Give the preparation type.
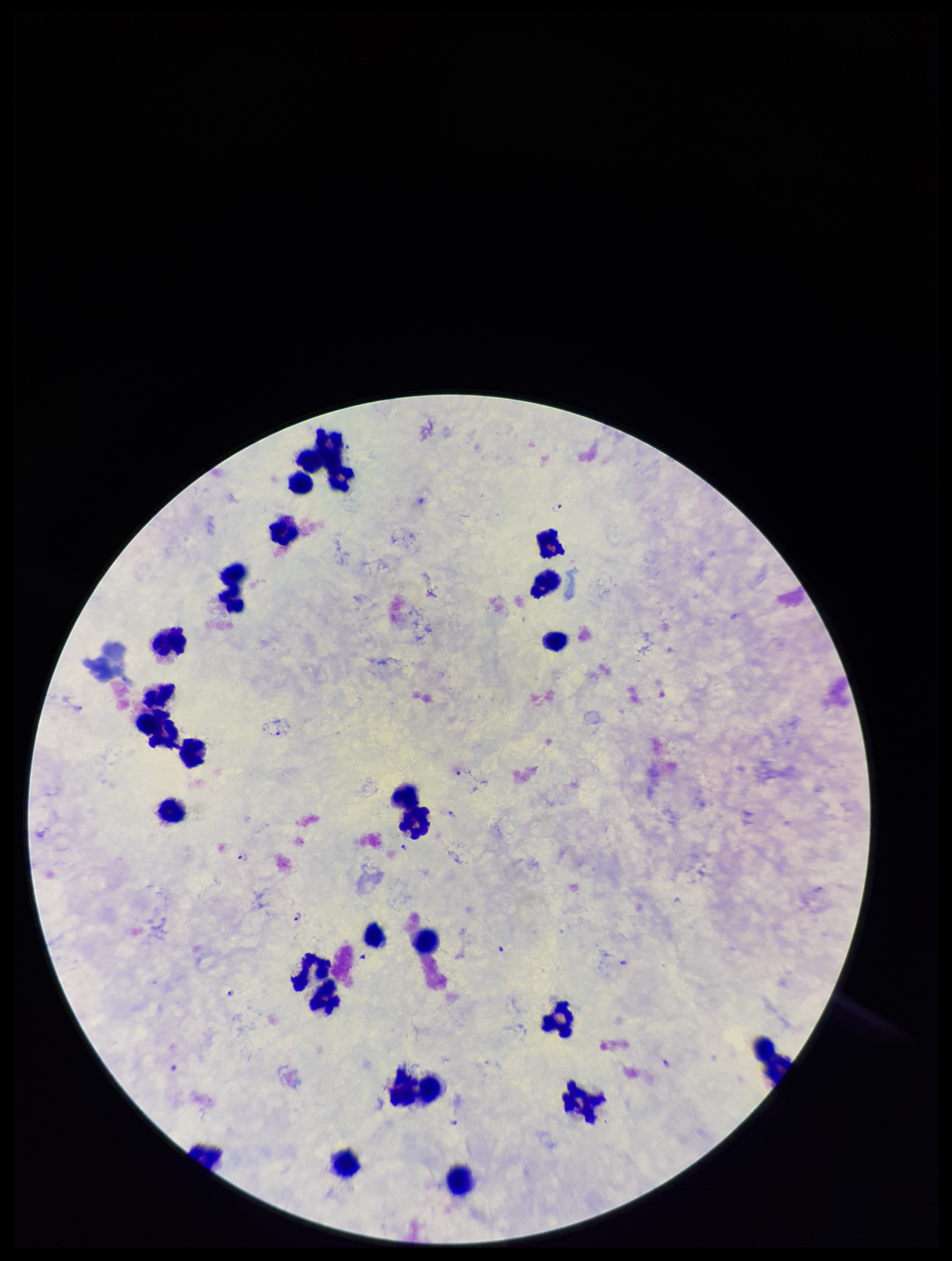
It is a thick blood smear.

One field from this slide. Parasite count: 12. Species reported for this patient: Plasmodium falciparum. Stained with Giemsa. Leukocyte count: 26. Plasmodium parasites: detected. Smartphone photograph taken through the eyepiece of a microscope. Image is 952×1261 pixels. Patient malaria status: infected.